Name the parasite shown.
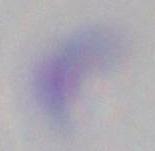
Toxoplasma gondii.

Summary:
  - Modality: micrograph
  - Magnification: 1000x